Assess this cell for malaria.
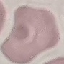

It is uninfected.

{
  "preparation": "thin smear",
  "stain": "Giemsa",
  "capture": "smartphone camera at the microscope eyepiece",
  "image_type": "cell patch, automatically extracted from a larger field of view and resized to 64 × 64 pixels"
}